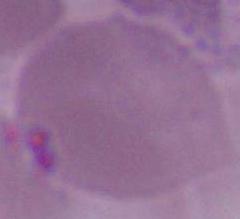
{
  "magnification": "1000x",
  "identification": "erythrocyte",
  "modality": "photomicrograph"
}